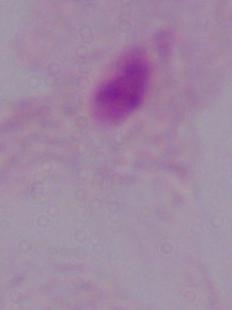
Summary:
  - Magnification: 1000x
  - Modality: micrograph
  - Identification: trichomonad